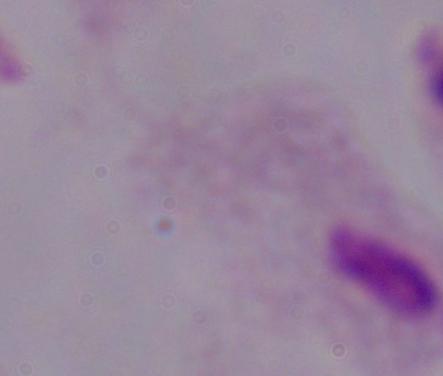

modality = micrograph
magnification = 1000x
identification = trichomonad